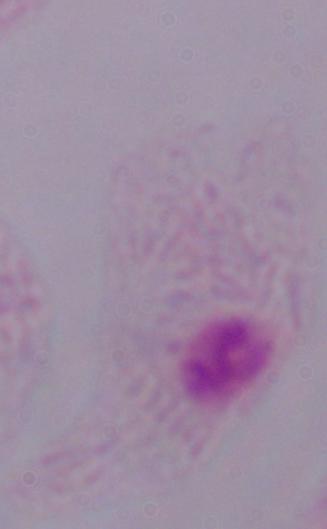

Summary:
  - Modality: photomicrograph
  - Magnification: 1000x
  - Identification: trichomonad